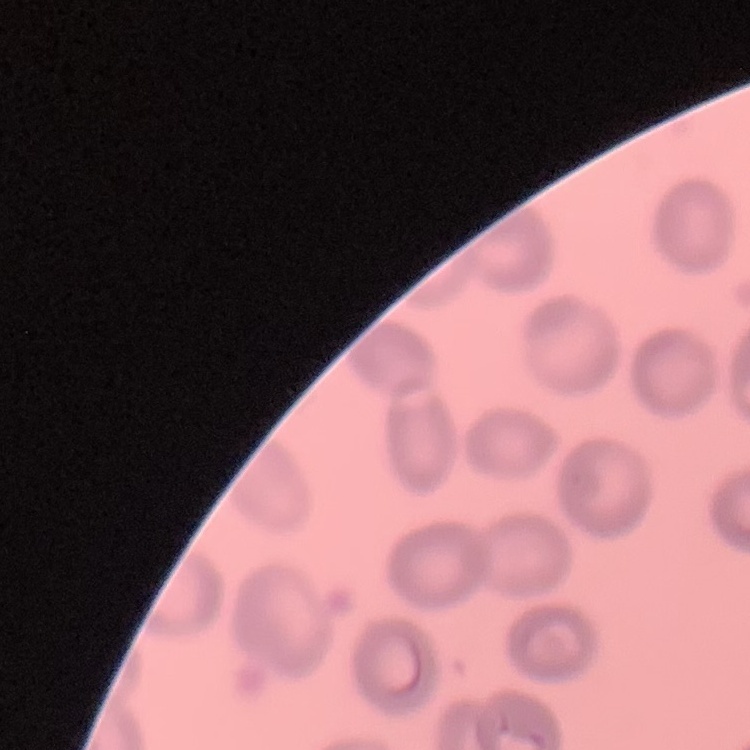

Summary:
  - Red blood cell morphology: no rouleaux formation
  - Stain: Field's or Giemsa
  - Image type: square crop of a larger photomicrograph
  - Preparation: thin blood smear